Assess this cell for malaria.
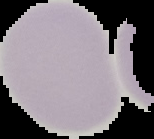
It is uninfected.

The area outside the segmented cell region is set to black. Image is 154×139 pixels. From a thin blood film.